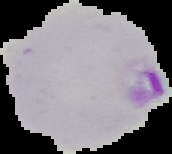
result = Plasmodium parasites detected
image size = 172×154 pixels
image type = cell region segmented out of the field of view; surrounding area masked to black
preparation = thin blood smear